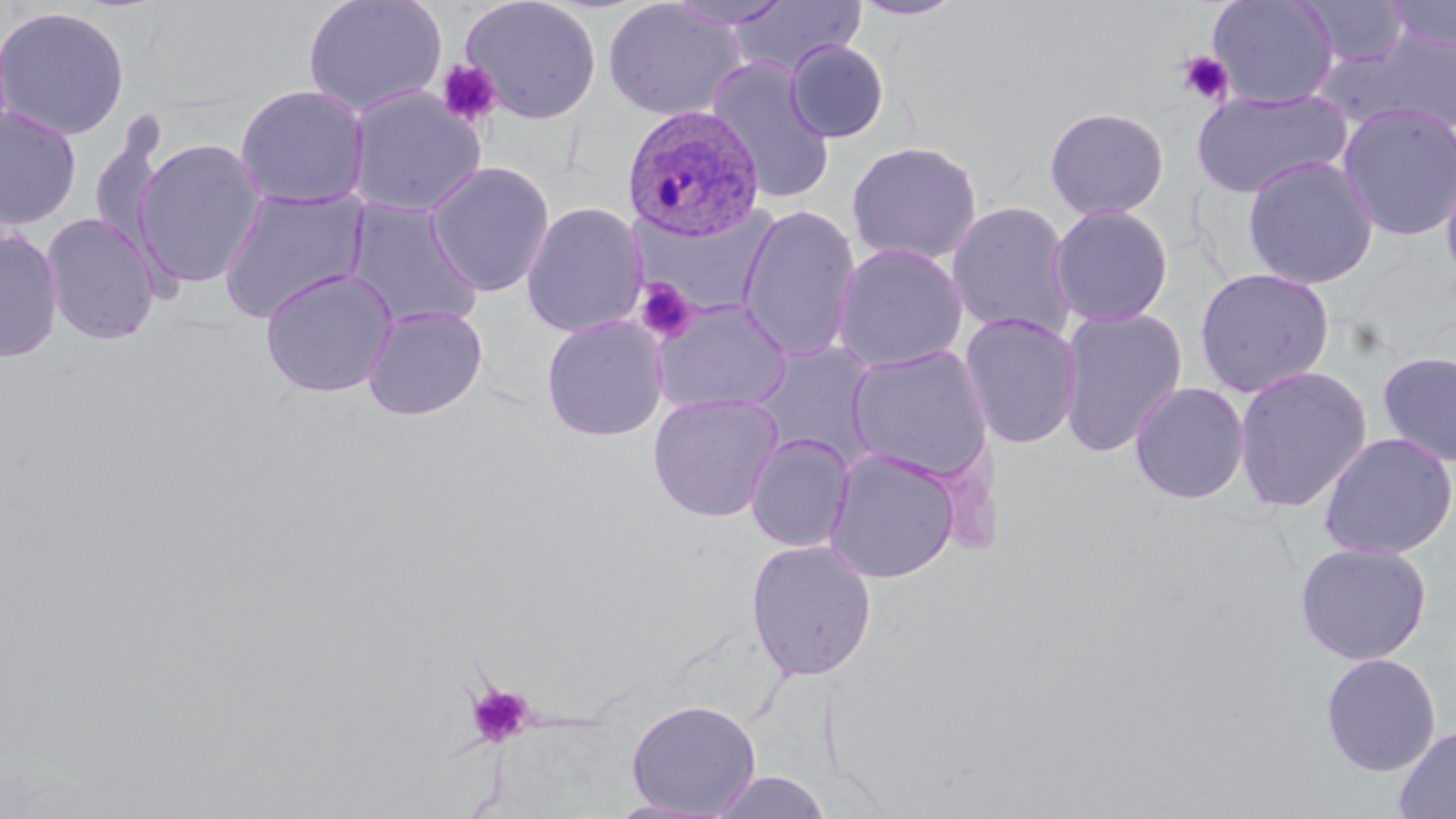

Summary:
  - Coordinate format: approximate bounding boxes as (x1,y1)-(x2,y2) corner pairs in pixels
  - Platelet locations: (1176,51)-(1234,105), (436,59)-(502,128), (633,278)-(697,343), (467,684)-(534,748)
  - Uninfected red blood cell locations: (303,0)-(448,118), (459,0)-(603,125), (602,0)-(744,122), (664,0)-(795,31), (850,0)-(970,21), (1207,0)-(1339,109), (1298,0)-(1409,69), (1383,0)-(1455,53), (727,1)-(867,78), (0,6)-(130,141), (1325,29)-(1456,138), (785,39)-(890,143), (705,57)-(837,205), (234,84)-(370,211), (346,86)-(487,219), (1191,87)-(1350,198), (1336,102)-(1456,242), (0,106)-(82,231), (1043,106)-(1170,220), (87,115)-(170,256), (133,138)-(268,287), (845,140)-(983,265), (1439,151)-(1456,290), (1242,154)-(1379,290), (425,161)-(555,297), (217,186)-(370,323), (344,198)-(484,332), (630,200)-(782,320), (946,200)-(1078,341), (521,202)-(648,337), (1048,203)-(1174,328), (737,204)-(862,362), (41,212)-(162,346), (0,228)-(64,364), (832,242)-(969,373), (1194,266)-(1335,398), (259,268)-(398,398), (651,297)-(793,415), (362,304)-(489,421), (1057,306)-(1189,458), (958,310)-(1083,450), (540,315)-(669,441), (749,339)-(880,464), (846,344)-(995,484), (1376,349)-(1456,468), (1233,365)-(1372,513), (1129,381)-(1251,505), (647,392)-(784,522), (745,432)-(855,553), (1318,432)-(1456,560), (823,447)-(961,585), (746,538)-(877,681), (1294,541)-(1433,666), (1319,652)-(1442,777), (625,698)-(761,816), (1394,724)-(1456,818), (708,771)-(832,818)
  - Plasmodium ovale-infected red blood cell locations: (622,104)-(766,240)
  - Slide-level diagnosis: Plasmodium ovale
  - Magnification: 1000x
  - Modality: light microscopy
  - Stain: May-Grünwald-Giemsa
  - Field of view: single
  - Image size: 1456×819 pixels
  - Preparation: thin blood smear